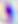

Summary:
  - Identification: Toxoplasma gondii
  - Modality: micrograph
  - Magnification: 400x